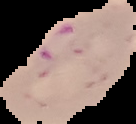
Cell region segmented out of the field of view; the surrounding area is masked to black. Image is 136×124 pixels. Malaria status: parasitized. From a thin blood smear.